Locate platelets.
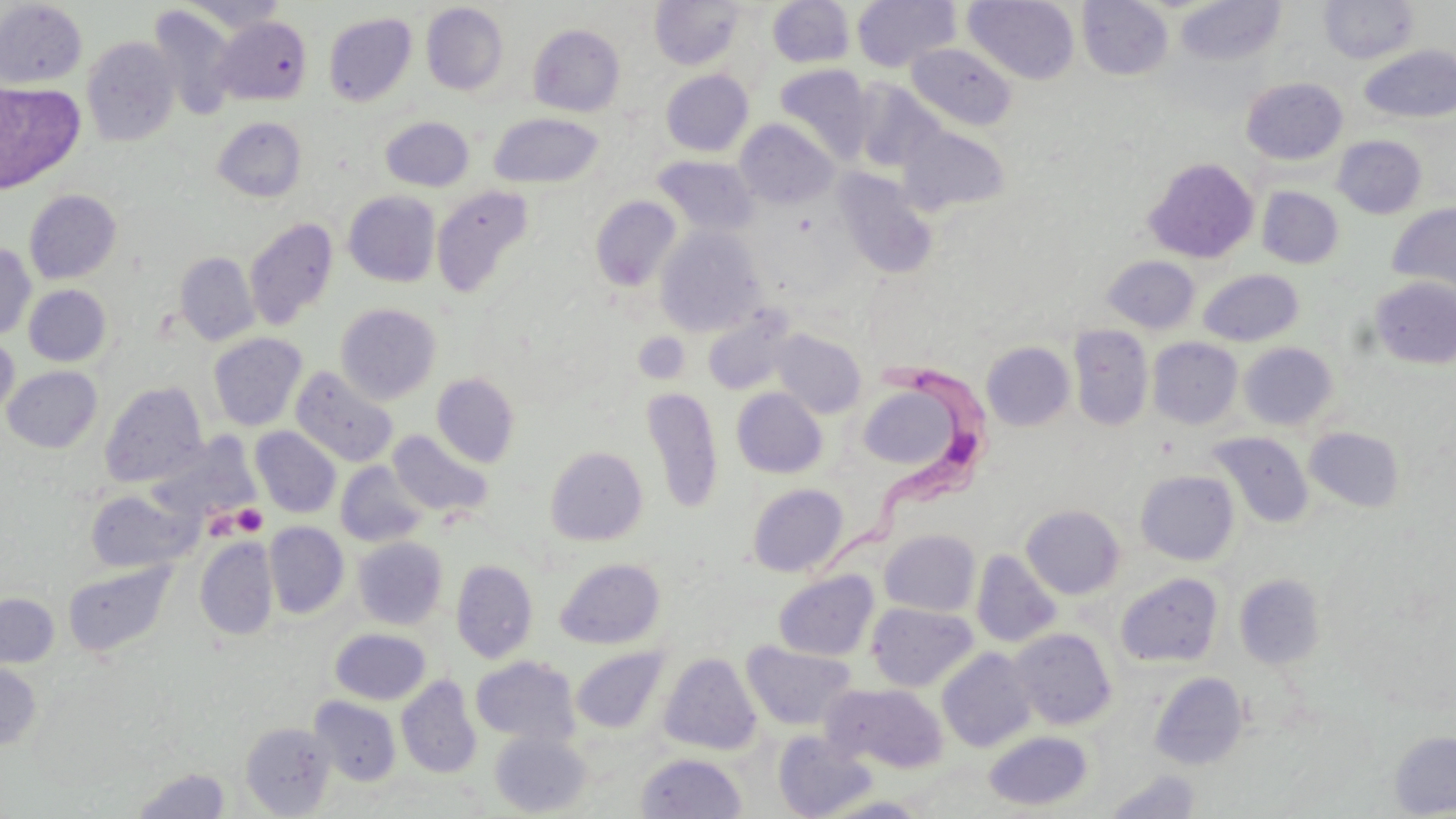

Approximate bounding boxes as named x1/y1/x2/y2 corners in pixels.
Platelets: (x1=634, y1=331, x2=690, y2=384), (x1=231, y1=504, x2=267, y2=536).

Trypanosoma brucei locations = approximate bounding boxes as named x1/y1/x2/y2 corners in pixels: (x1=819, y1=352, x2=1000, y2=597)
slide-level diagnosis = Trypanosoma brucei
modality = optical microscopy
image size = 1456×819 pixels
magnification = 1000x
stain = May-Grünwald-Giemsa
uninfected red blood cell locations = approximate bounding boxes as named x1/y1/x2/y2 corners in pixels: (x1=767, y1=0, x2=855, y2=68), (x1=852, y1=0, x2=960, y2=72), (x1=964, y1=0, x2=1080, y2=84), (x1=1077, y1=0, x2=1173, y2=80), (x1=0, y1=1, x2=87, y2=88), (x1=180, y1=1, x2=288, y2=34), (x1=650, y1=1, x2=745, y2=70), (x1=1176, y1=1, x2=1287, y2=67), (x1=1318, y1=1, x2=1420, y2=64), (x1=421, y1=3, x2=509, y2=96), (x1=147, y1=5, x2=239, y2=120), (x1=323, y1=12, x2=417, y2=106), (x1=213, y1=16, x2=312, y2=105), (x1=528, y1=24, x2=625, y2=116), (x1=82, y1=36, x2=181, y2=147), (x1=906, y1=42, x2=1017, y2=130), (x1=1358, y1=45, x2=1456, y2=124), (x1=774, y1=64, x2=873, y2=163), (x1=661, y1=70, x2=753, y2=157), (x1=1241, y1=77, x2=1348, y2=165), (x1=851, y1=79, x2=945, y2=173), (x1=0, y1=80, x2=24, y2=173), (x1=0, y1=83, x2=84, y2=193), (x1=488, y1=113, x2=604, y2=189), (x1=381, y1=116, x2=474, y2=192), (x1=213, y1=117, x2=307, y2=202), (x1=736, y1=119, x2=838, y2=209), (x1=898, y1=125, x2=1010, y2=215), (x1=1332, y1=135, x2=1426, y2=218), (x1=655, y1=156, x2=759, y2=236), (x1=1143, y1=157, x2=1259, y2=263), (x1=834, y1=170, x2=938, y2=278), (x1=431, y1=185, x2=535, y2=299), (x1=1257, y1=186, x2=1343, y2=268), (x1=25, y1=190, x2=122, y2=284), (x1=343, y1=191, x2=441, y2=286), (x1=590, y1=195, x2=681, y2=292), (x1=1387, y1=202, x2=1456, y2=298), (x1=244, y1=218, x2=339, y2=330), (x1=654, y1=226, x2=766, y2=337), (x1=0, y1=242, x2=36, y2=341), (x1=174, y1=251, x2=259, y2=346), (x1=1103, y1=256, x2=1200, y2=333), (x1=1199, y1=269, x2=1304, y2=346), (x1=1371, y1=277, x2=1456, y2=369), (x1=23, y1=285, x2=111, y2=366), (x1=335, y1=303, x2=442, y2=404), (x1=702, y1=309, x2=797, y2=396), (x1=1069, y1=325, x2=1153, y2=431), (x1=770, y1=329, x2=867, y2=418), (x1=634, y1=332, x2=691, y2=383), (x1=208, y1=333, x2=307, y2=431), (x1=0, y1=336, x2=19, y2=420), (x1=1148, y1=337, x2=1243, y2=429), (x1=981, y1=341, x2=1075, y2=431), (x1=1238, y1=342, x2=1338, y2=431), (x1=3, y1=365, x2=102, y2=453), (x1=290, y1=366, x2=398, y2=467), (x1=431, y1=373, x2=520, y2=467), (x1=100, y1=381, x2=208, y2=487), (x1=856, y1=381, x2=971, y2=474), (x1=642, y1=387, x2=724, y2=514), (x1=732, y1=388, x2=827, y2=478), (x1=250, y1=426, x2=341, y2=518), (x1=1304, y1=427, x2=1405, y2=513), (x1=387, y1=429, x2=494, y2=519), (x1=1207, y1=431, x2=1313, y2=528), (x1=147, y1=436, x2=259, y2=527), (x1=545, y1=445, x2=648, y2=545), (x1=335, y1=461, x2=428, y2=547), (x1=1136, y1=470, x2=1239, y2=565), (x1=747, y1=483, x2=848, y2=577), (x1=86, y1=489, x2=199, y2=573), (x1=1021, y1=504, x2=1125, y2=599), (x1=263, y1=522, x2=349, y2=618), (x1=878, y1=529, x2=981, y2=616), (x1=195, y1=537, x2=278, y2=640), (x1=353, y1=537, x2=447, y2=629), (x1=972, y1=550, x2=1062, y2=648), (x1=555, y1=558, x2=665, y2=649), (x1=451, y1=560, x2=538, y2=663), (x1=63, y1=561, x2=176, y2=658), (x1=774, y1=570, x2=878, y2=661), (x1=1115, y1=572, x2=1223, y2=668), (x1=1235, y1=574, x2=1326, y2=670), (x1=0, y1=593, x2=59, y2=668), (x1=866, y1=602, x2=977, y2=692), (x1=330, y1=628, x2=431, y2=705), (x1=1010, y1=628, x2=1116, y2=730), (x1=742, y1=642, x2=857, y2=731), (x1=570, y1=646, x2=670, y2=734), (x1=937, y1=647, x2=1037, y2=752), (x1=659, y1=653, x2=761, y2=755), (x1=471, y1=655, x2=580, y2=746), (x1=0, y1=661, x2=42, y2=752), (x1=1150, y1=672, x2=1248, y2=770), (x1=396, y1=675, x2=482, y2=779), (x1=824, y1=682, x2=949, y2=773), (x1=310, y1=696, x2=401, y2=786), (x1=240, y1=722, x2=336, y2=817), (x1=983, y1=730, x2=1094, y2=811), (x1=1389, y1=730, x2=1456, y2=817), (x1=490, y1=731, x2=591, y2=817), (x1=773, y1=731, x2=878, y2=819), (x1=637, y1=752, x2=746, y2=818), (x1=133, y1=767, x2=231, y2=817), (x1=1106, y1=769, x2=1201, y2=818)
preparation = thin blood film
field of view = single